Identify the cell.
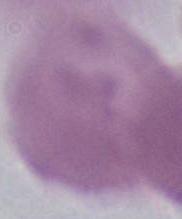
An erythrocyte.

{
  "magnification": "1000x",
  "modality": "photomicrograph"
}